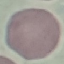
{
  "result": "no malaria parasites seen",
  "image_type": "cell patch, automatically extracted from a larger field of view and resized to 64 × 64 pixels",
  "stain": "Giemsa",
  "preparation": "thin blood film",
  "capture": "smartphone camera at the microscope eyepiece"
}